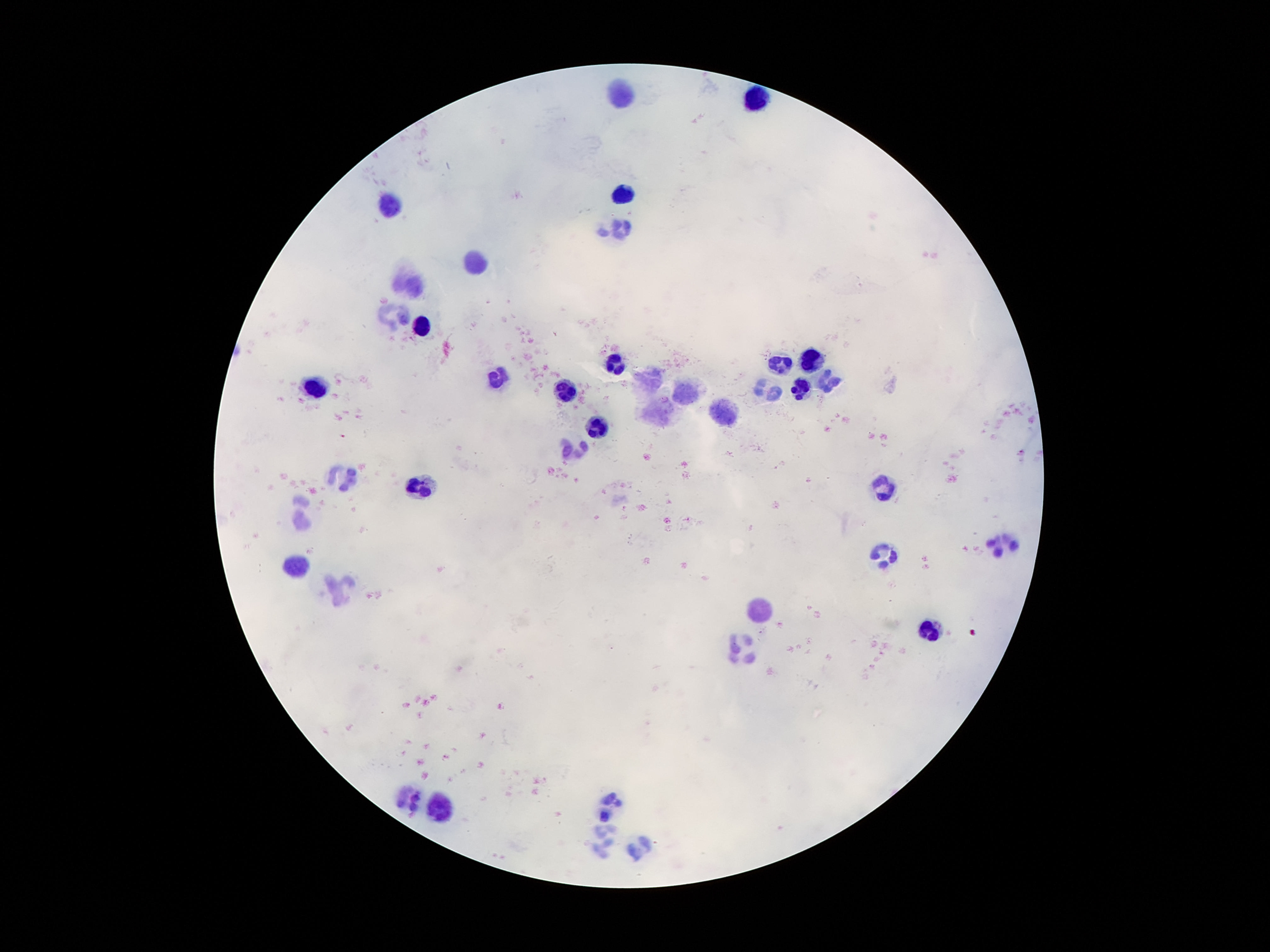

Approximate centers as (x, y) in pixels.
Summary:
  - Leukocyte locations: (622, 93), (755, 98), (623, 195), (393, 203), (620, 230), (478, 261), (411, 283), (393, 313), (421, 329), (811, 358), (615, 363), (781, 365), (501, 378), (826, 383), (651, 385), (801, 386), (315, 389), (770, 390), (565, 391), (689, 391), (658, 411), (725, 412), (595, 427), (572, 452), (341, 475), (421, 482), (887, 486), (300, 510), (999, 546), (885, 555), (295, 565), (337, 588), (765, 608), (929, 633), (744, 654), (409, 798), (612, 804), (442, 807), (602, 844), (642, 848)
  - Capture: smartphone camera through the microscope eyepiece
  - Magnification: 100x
  - Stain: Giemsa
  - Image size: 1270×952 pixels
  - Patient malaria status: not infected
  - Field of view: single
  - Preparation: thick blood smear